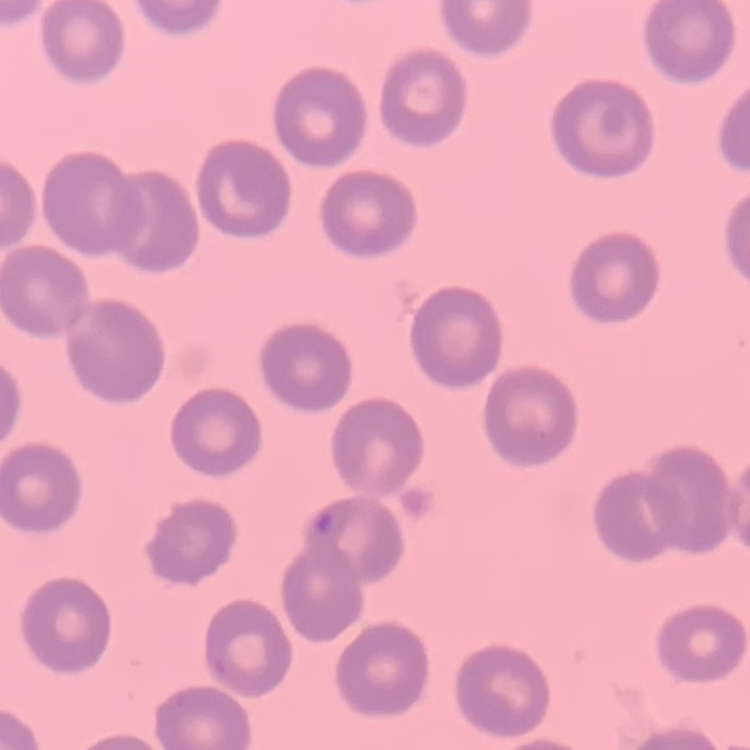

red_blood_cell_morphology: no rouleaux formation
stain: Field's or Giemsa
preparation: thin blood smear
image_type: one tile cut from a larger photomicrograph